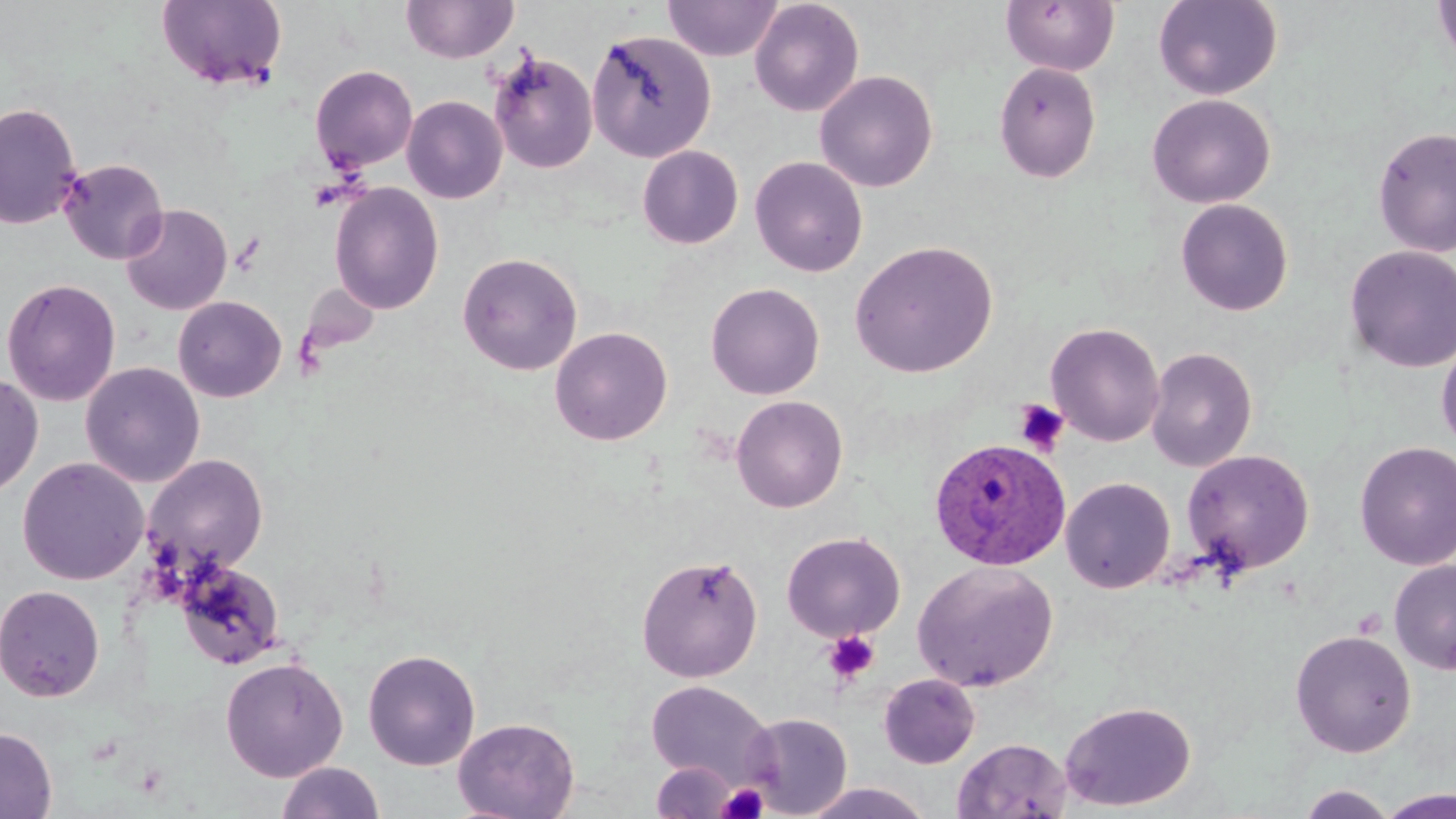

Summary:
  - Coordinate format: approximate bounding boxes as [x1, y1, x2, y2] in pixels
  - Platelet locations: [1013, 399, 1070, 455], [823, 630, 880, 685], [716, 782, 771, 818]
  - Plasmodium ovale-infected red blood cell locations: [929, 437, 1070, 570]
  - Uninfected red blood cell locations: [401, 0, 519, 64], [663, 0, 782, 61], [749, 0, 865, 117], [1001, 0, 1119, 76], [1153, 0, 1283, 100], [1432, 0, 1456, 72], [157, 1, 287, 91], [587, 28, 716, 163], [487, 50, 598, 174], [994, 62, 1101, 183], [309, 64, 418, 173], [814, 70, 938, 192], [1147, 94, 1275, 209], [402, 95, 507, 204], [0, 102, 83, 230], [1372, 126, 1456, 258], [637, 145, 743, 249], [750, 156, 868, 277], [59, 158, 169, 265], [329, 182, 444, 315], [1175, 198, 1293, 316], [120, 204, 232, 315], [849, 240, 998, 378], [1344, 245, 1456, 373], [457, 251, 583, 375], [1, 277, 121, 407], [298, 282, 379, 358], [706, 282, 824, 399], [173, 296, 287, 402], [1045, 322, 1166, 447], [550, 326, 673, 445], [1436, 335, 1456, 454], [1145, 346, 1258, 472], [81, 361, 205, 487], [0, 373, 43, 498], [731, 395, 848, 513], [1354, 440, 1456, 571], [1182, 449, 1315, 575], [143, 454, 269, 577], [17, 457, 149, 585], [1061, 477, 1175, 593], [782, 531, 905, 641], [636, 554, 763, 682], [175, 559, 286, 670], [1389, 559, 1456, 675], [912, 560, 1059, 693], [0, 584, 105, 702], [1290, 629, 1417, 757], [363, 648, 481, 771], [220, 657, 348, 781], [878, 673, 980, 768], [645, 680, 777, 790], [1060, 701, 1196, 811], [742, 712, 852, 817], [453, 717, 580, 819], [0, 726, 58, 818], [952, 737, 1073, 818], [651, 760, 743, 818], [276, 762, 386, 819], [800, 781, 935, 818], [1294, 784, 1399, 819], [1379, 788, 1456, 818]
  - Slide-level diagnosis: Plasmodium ovale
  - Stain: May-Grünwald-Giemsa
  - Magnification: 1000x
  - Modality: optical microscopy
  - Preparation: thin blood film
  - Field of view: single
  - Image size: 1456×819 pixels